Identify the blood parasite species.
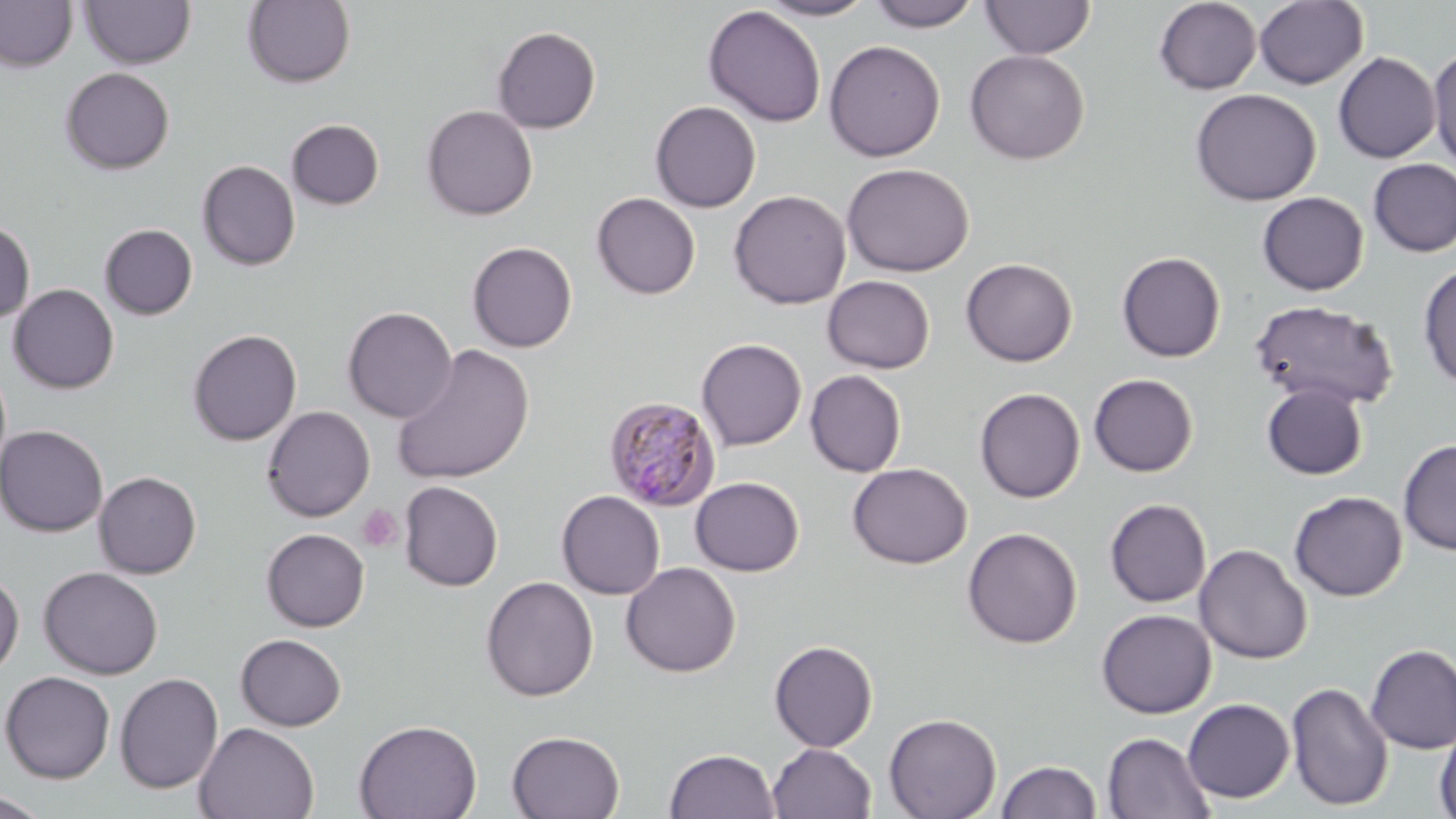

Plasmodium malariae.

Approximate bounding boxes as (x1,y1)-(x2,y2) corner pairs in pixels. Platelet locations: (357,504)-(402,552). Plasmodium malariae-infected red blood cell locations: (604,396)-(722,512). Uninfected red blood cell locations: (0,0)-(79,72), (867,0)-(982,32), (1153,0)-(1262,94), (1254,0)-(1369,89), (80,1)-(196,70), (242,1)-(356,88), (758,1)-(877,21), (980,1)-(1096,59), (703,5)-(826,127), (492,26)-(601,133), (824,40)-(945,161), (1428,46)-(1456,171), (964,49)-(1090,165), (1333,51)-(1441,163), (60,67)-(175,175), (1189,88)-(1321,206), (650,100)-(761,212), (421,104)-(538,220), (287,118)-(385,210), (1369,159)-(1456,257), (197,160)-(301,271), (841,162)-(974,277), (728,189)-(851,309), (1257,191)-(1369,295), (591,192)-(700,299), (0,220)-(35,323), (100,224)-(198,320), (467,241)-(577,352), (1116,251)-(1226,362), (960,258)-(1078,367), (1418,263)-(1456,389), (822,275)-(935,374), (8,283)-(119,393), (1249,299)-(1400,411), (342,306)-(458,423), (187,329)-(302,446), (696,337)-(807,452), (392,343)-(534,485), (805,369)-(907,477), (1088,373)-(1198,476), (1261,383)-(1369,480), (974,387)-(1085,503), (262,406)-(375,522), (0,424)-(108,537), (1398,439)-(1456,555), (847,462)-(972,568), (93,471)-(202,578), (690,476)-(804,576), (399,481)-(503,591), (556,490)-(665,599), (1289,491)-(1407,601), (1104,498)-(1212,607), (962,526)-(1083,648), (261,527)-(370,631), (1194,543)-(1312,665), (620,561)-(741,678), (38,566)-(163,679), (0,570)-(24,677), (481,576)-(599,702), (1096,608)-(1216,718), (235,633)-(347,732), (769,640)-(878,752), (1365,644)-(1456,754), (1,671)-(115,784), (114,672)-(224,794), (1286,680)-(1394,812), (1182,698)-(1295,803), (884,712)-(1001,819), (353,719)-(482,819), (194,722)-(320,819), (1434,724)-(1456,819), (507,730)-(626,818), (1102,731)-(1215,819), (767,743)-(876,819), (663,748)-(781,819), (995,759)-(1102,819), (0,791)-(51,818). Thin blood smear. Optical microscopy. Image is 1456×819 pixels. May-Grünwald-Giemsa stain. Single field of view. Captured at 1000x magnification.